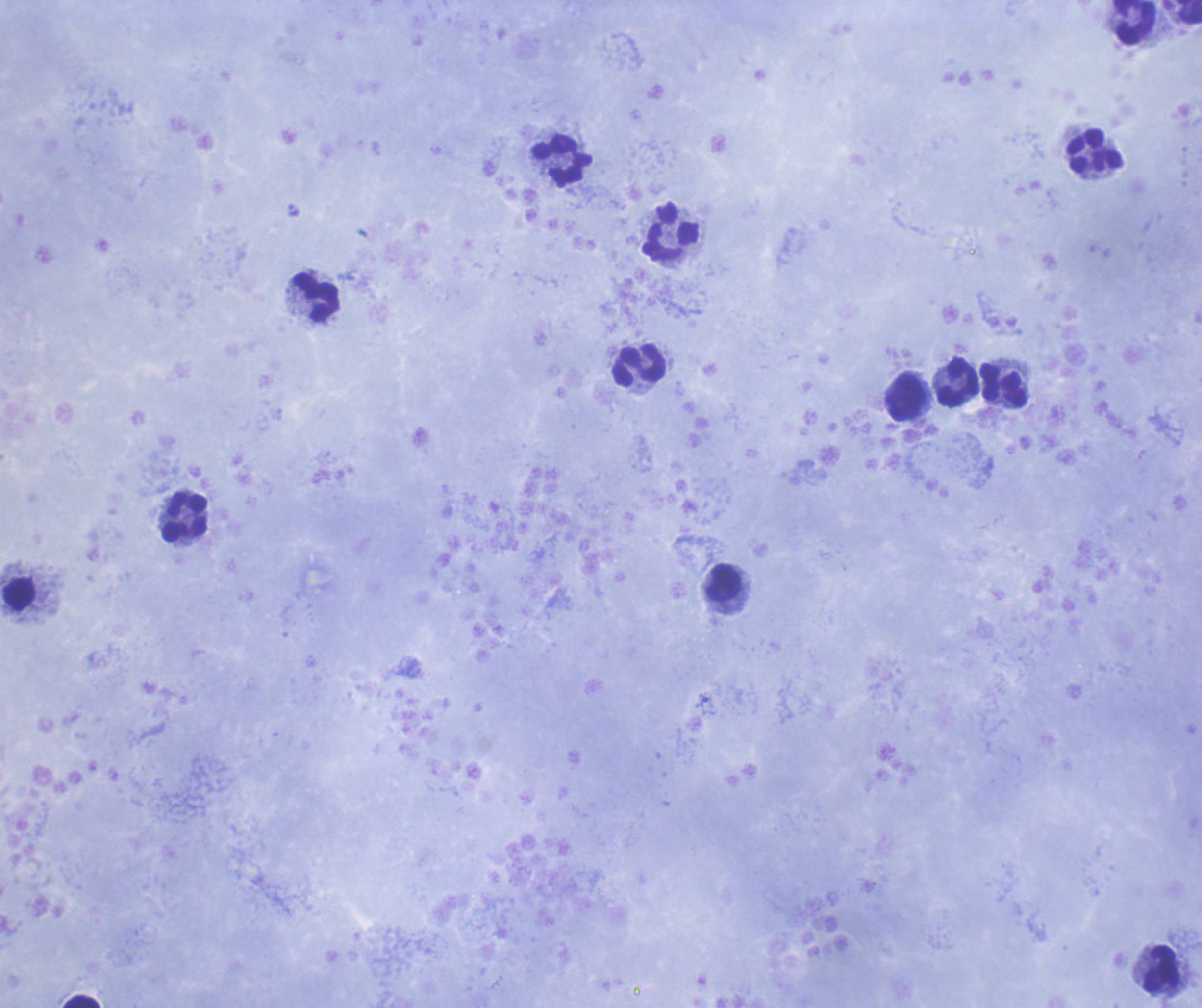 Approximate centers as [x, y] in pixels. Leukocyte locations: [1188, 12], [1135, 22], [1096, 150], [561, 161], [671, 233], [317, 298], [638, 366], [958, 381], [1003, 386], [905, 397], [185, 517], [723, 582], [20, 594], [1160, 969], [81, 1002]. Single field of view. Coloration quality: good. Captured at 100x magnification. Previously used in a real diagnosis. Thick blood film. Image is 1202×1008 pixels. Romanowsky stain. Result: no Plasmodium parasites seen. Background quality: good.